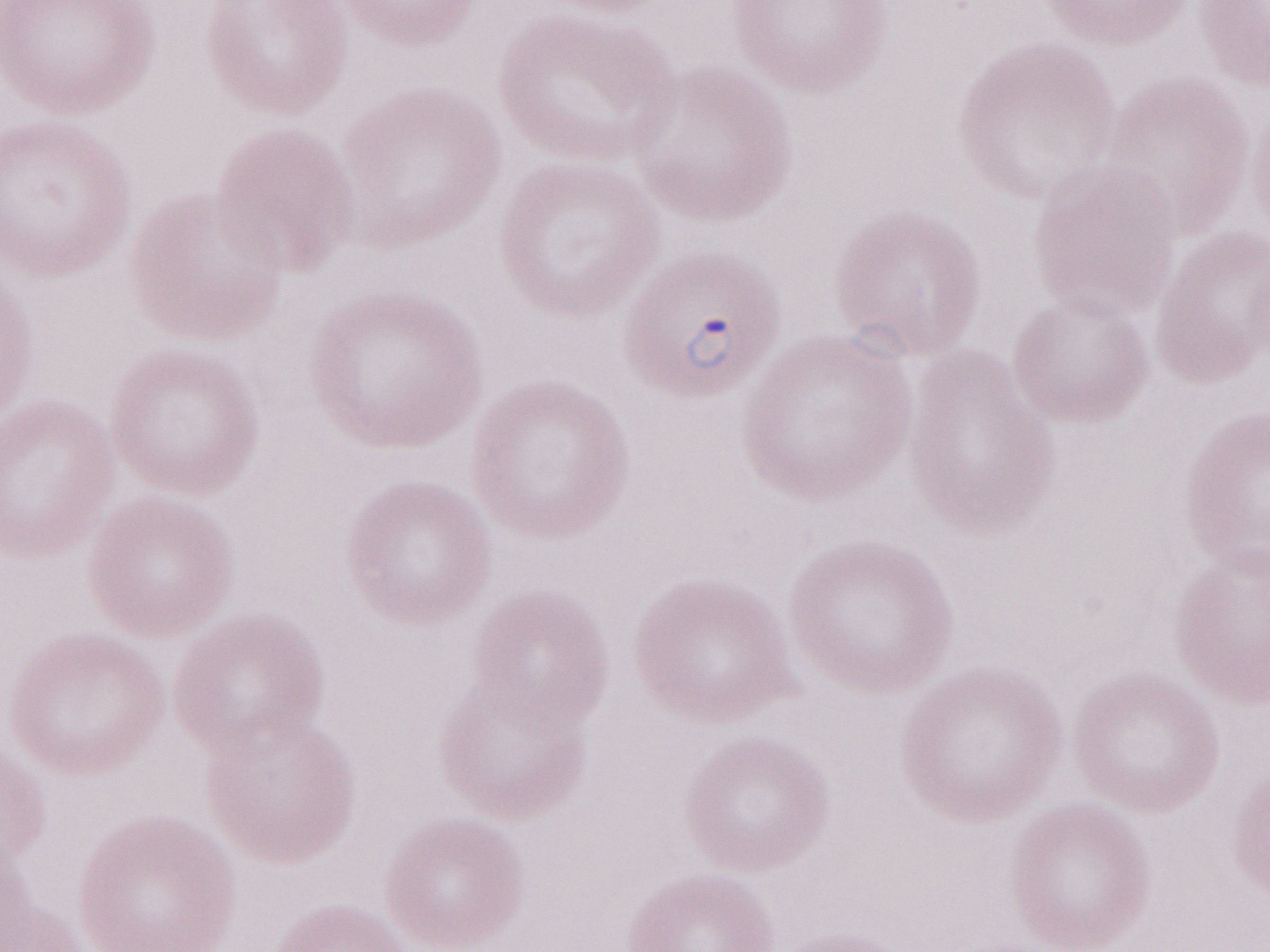 Patient diagnosis: malaria infection. Image is 1270×952 pixels. Single field of view. Thin peripheral-blood smear. Olympus BX43 microscope, Olympus DP73 camera. 1,000x magnification. May-Grünwald-Giemsa (MGG) stain.